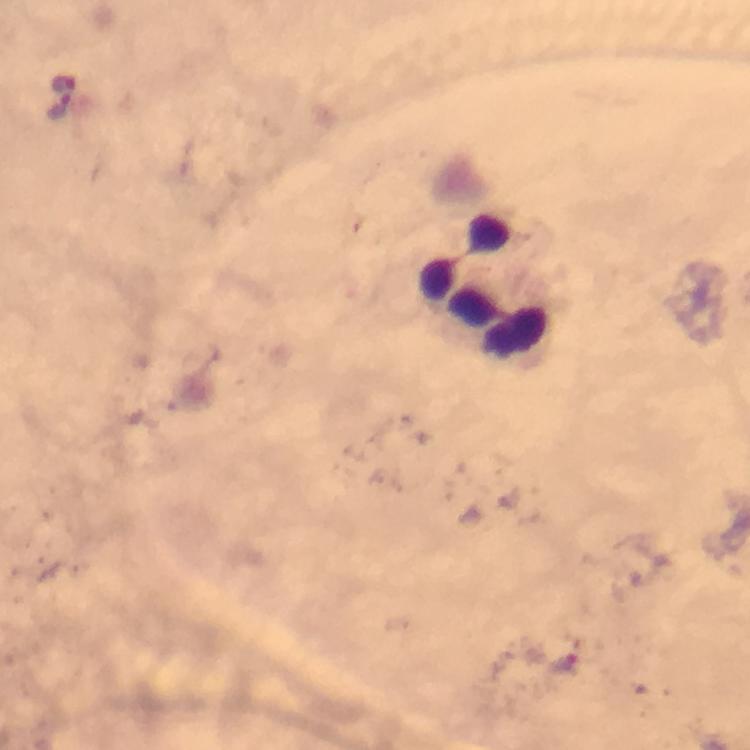
Approximate centers as [x, y] in pixels. Malaria parasite locations: [62, 82], [63, 105], [564, 665]. Leukocyte locations: [485, 288]. Immersion oil was used. Cropped region of a single field of view. Image is 750×750 pixels. Thick blood smear. Photographed with a smartphone mounted on the microscope. From a diagnostic examination for malaria. Giemsa-stained preparation. At 100x magnification.